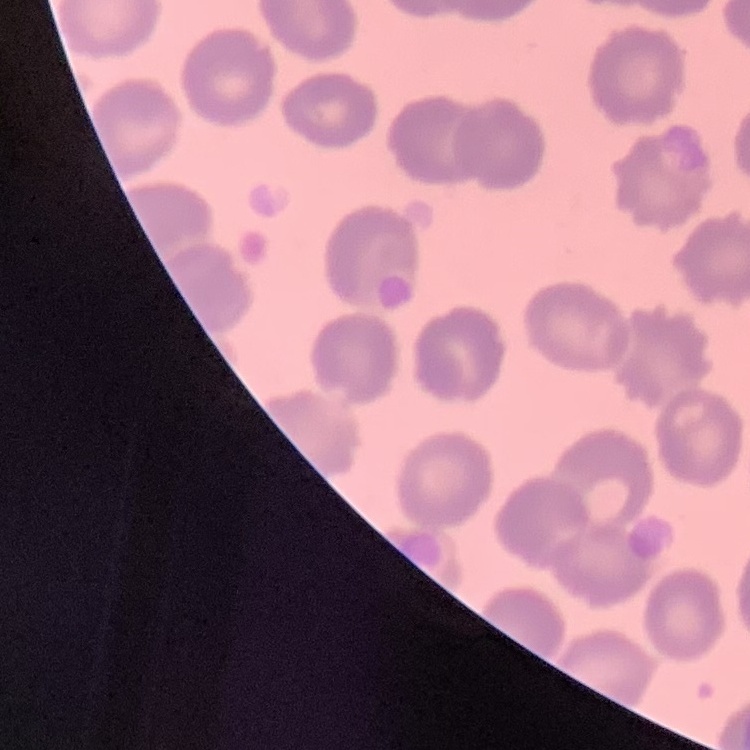
red_blood_cell_morphology: no rouleaux formation
image_type: one tile cut from a larger photomicrograph
stain: Field's or Giemsa
preparation: thin blood film